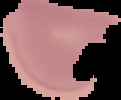
Summary:
  - Image type: segmented cell region on a black background
  - Preparation: thin blood smear
  - Image size: 121×100 pixels
  - Result: no malaria parasites seen